Assess this cell for malaria.
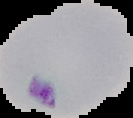
Parasitized.

Image is 133×118 pixels. Segmented cell region on a black background. From a thin blood smear.